Name the cell type shown.
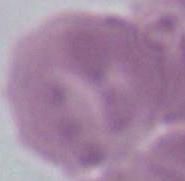

An erythrocyte.

Summary:
  - Magnification: 1000x
  - Modality: micrograph